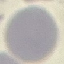

Summary:
  - Malaria status: uninfected
  - Image type: cell patch, automatically extracted from a larger field of view and resized to 64 × 64 pixels
  - Preparation: thin blood film
  - Capture: smartphone camera at the microscope eyepiece
  - Stain: Giemsa